Identify the blood parasite species.
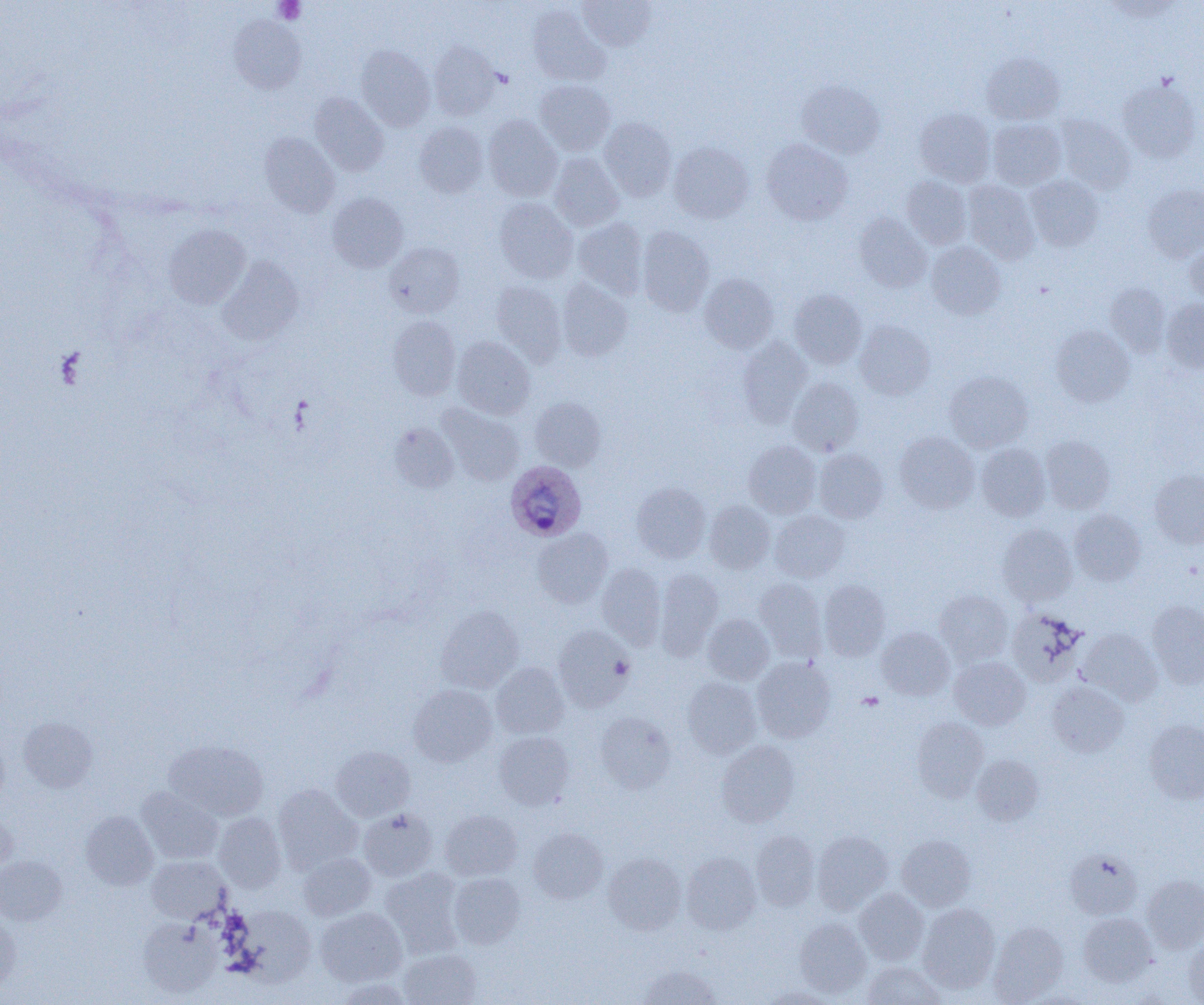

Plasmodium ovale.

Approximate bounding boxes as (x1, y1, x2, y2) in pixels. Uninfected red blood cell locations: (577, 0, 656, 50), (1102, 1, 1185, 22), (528, 4, 609, 86), (229, 16, 306, 94), (428, 42, 500, 120), (356, 45, 435, 130), (982, 52, 1064, 124), (1117, 77, 1201, 163), (534, 79, 615, 155), (796, 80, 885, 158), (310, 92, 388, 176), (914, 107, 995, 187), (483, 115, 563, 201), (1056, 115, 1134, 193), (599, 117, 677, 201), (988, 119, 1066, 190), (414, 122, 488, 197), (259, 132, 339, 217), (761, 139, 852, 225), (669, 141, 754, 223), (549, 153, 624, 231), (902, 176, 972, 248), (1025, 176, 1103, 251), (963, 180, 1040, 264), (1142, 183, 1204, 262), (327, 192, 408, 272), (493, 198, 578, 283), (854, 213, 931, 292), (574, 217, 648, 298), (163, 224, 250, 309), (637, 226, 715, 316), (1185, 240, 1204, 306), (926, 241, 1006, 319), (384, 242, 464, 318), (217, 257, 304, 345), (699, 273, 778, 353), (557, 279, 633, 362), (491, 281, 566, 364), (1105, 283, 1170, 356), (788, 289, 867, 369), (1162, 298, 1204, 373), (387, 316, 460, 399), (854, 320, 935, 400), (1050, 325, 1134, 406), (452, 336, 535, 419), (737, 337, 812, 427), (944, 370, 1033, 452), (788, 377, 864, 455), (530, 396, 606, 471), (438, 404, 524, 486), (388, 422, 459, 493), (894, 432, 979, 513), (1041, 436, 1114, 513), (744, 440, 821, 518), (976, 443, 1050, 521), (814, 449, 888, 523), (1149, 469, 1204, 548), (632, 482, 711, 563), (705, 500, 775, 573), (1069, 509, 1145, 585), (769, 510, 850, 582), (997, 524, 1077, 606), (532, 528, 613, 608), (554, 536, 643, 624), (596, 563, 666, 647), (655, 568, 723, 655), (754, 577, 826, 658), (819, 580, 890, 660), (934, 590, 1013, 665), (1147, 600, 1204, 688), (436, 605, 523, 693), (1007, 608, 1086, 686), (703, 614, 774, 684), (552, 626, 633, 711), (876, 627, 955, 699), (1079, 628, 1162, 704), (752, 657, 836, 743), (949, 657, 1030, 730), (491, 662, 569, 739), (682, 677, 761, 757), (1047, 682, 1128, 756), (408, 684, 497, 766), (595, 712, 676, 792), (19, 717, 97, 792), (912, 717, 988, 800), (1144, 720, 1204, 804), (494, 731, 574, 809), (0, 736, 9, 807), (165, 739, 269, 821), (716, 741, 800, 826), (331, 745, 415, 821), (972, 755, 1043, 825), (273, 784, 362, 873), (136, 787, 223, 864), (359, 808, 437, 881), (440, 809, 522, 880), (0, 810, 17, 876), (80, 811, 158, 889), (213, 813, 286, 893), (528, 827, 608, 904), (750, 830, 820, 911), (812, 831, 893, 912), (897, 835, 976, 910), (1066, 849, 1142, 919), (681, 852, 761, 934), (299, 853, 376, 920), (603, 853, 686, 935), (146, 855, 230, 923), (0, 856, 66, 925), (380, 868, 465, 956), (449, 872, 526, 949), (1143, 875, 1204, 952), (853, 888, 929, 965), (917, 904, 1000, 993), (231, 906, 317, 985), (315, 907, 407, 987), (1078, 912, 1157, 986), (0, 915, 20, 993), (138, 917, 221, 998), (794, 917, 871, 997), (988, 921, 1068, 1004), (1184, 938, 1204, 1004), (399, 949, 481, 1005), (862, 961, 945, 1004), (637, 964, 720, 1005), (333, 977, 414, 1005), (759, 987, 841, 1004). Platelet locations: (273, 0, 305, 24), (611, 656, 633, 679), (857, 692, 884, 711). Plasmodium ovale-infected red blood cell locations: (505, 460, 586, 541). Image is 1204×1005 pixels. Thin blood smear. Single field of view. Light microscopy. 1000x magnification.